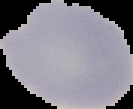

{
  "preparation": "thin blood film",
  "image_type": "segmented cell region with the area outside set to black",
  "malaria_status": "uninfected",
  "image_size": "133×109 pixels"
}